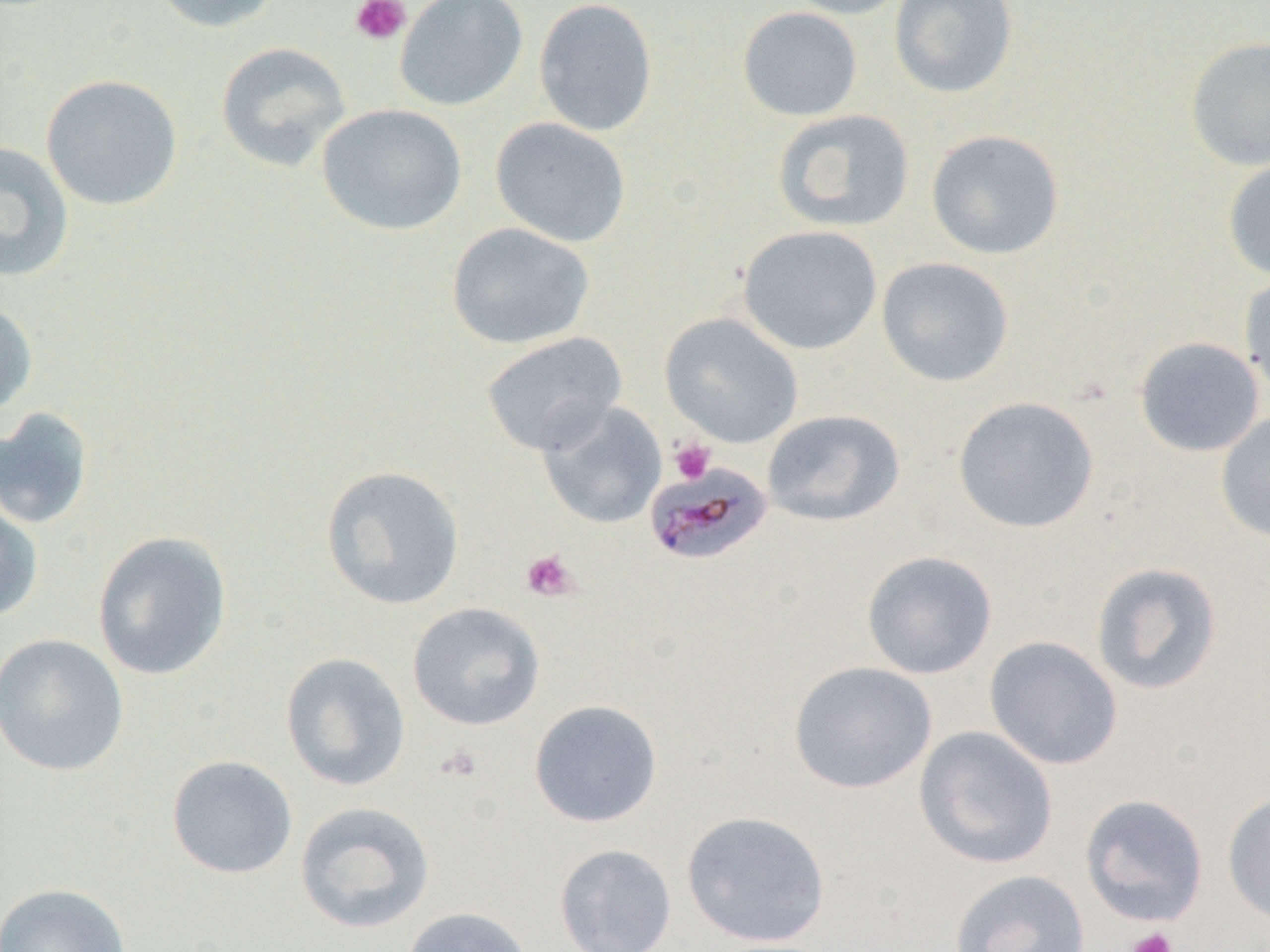

Summary:
  - Coordinate format: approximate bounding boxes as [x1, y1, x2, y2] in pixels
  - Platelet locations: [350, 0, 411, 46], [668, 438, 715, 484], [520, 549, 580, 601], [437, 744, 484, 783], [1126, 927, 1178, 952]
  - Uninfected red blood cell locations: [147, 0, 286, 34], [395, 0, 528, 111], [533, 0, 658, 137], [781, 0, 911, 19], [889, 0, 1018, 99], [737, 7, 863, 121], [1185, 36, 1270, 172], [215, 42, 351, 172], [41, 74, 183, 211], [317, 103, 467, 236], [772, 110, 915, 232], [490, 117, 631, 247], [926, 129, 1064, 259], [0, 140, 75, 283], [1222, 157, 1270, 282], [446, 223, 595, 350], [737, 225, 883, 355], [876, 256, 1014, 387], [1239, 270, 1270, 402], [0, 298, 37, 420], [660, 313, 803, 448], [480, 331, 627, 455], [1134, 337, 1264, 457], [953, 396, 1099, 534], [536, 401, 667, 529], [0, 407, 94, 530], [762, 409, 905, 527], [1215, 410, 1270, 543], [319, 465, 465, 610], [0, 490, 44, 624], [92, 530, 232, 682], [861, 550, 997, 679], [1090, 562, 1223, 696], [408, 602, 545, 730], [0, 633, 129, 777], [984, 636, 1123, 770], [280, 652, 411, 791], [788, 661, 937, 794], [529, 699, 663, 827], [914, 726, 1058, 869], [167, 755, 298, 879], [1222, 791, 1270, 925], [1080, 794, 1209, 927], [294, 801, 435, 934], [681, 810, 831, 947], [554, 844, 677, 952], [949, 869, 1090, 952], [1, 883, 132, 952], [400, 907, 534, 952]
  - Plasmodium malariae-infected red blood cell locations: [644, 460, 774, 567]
  - Slide-level diagnosis: Plasmodium malariae
  - Image size: 1270×952 pixels
  - Field of view: one of a larger specimen
  - Preparation: thin blood film
  - Magnification: 1000x
  - Modality: optical microscopy